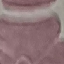

Result: no malaria parasites detected. Automatically extracted cell patch, resized to 64 × 64 pixels. Thin blood film. Photographed with a smartphone camera at the microscope eyepiece. Giemsa-stained preparation.